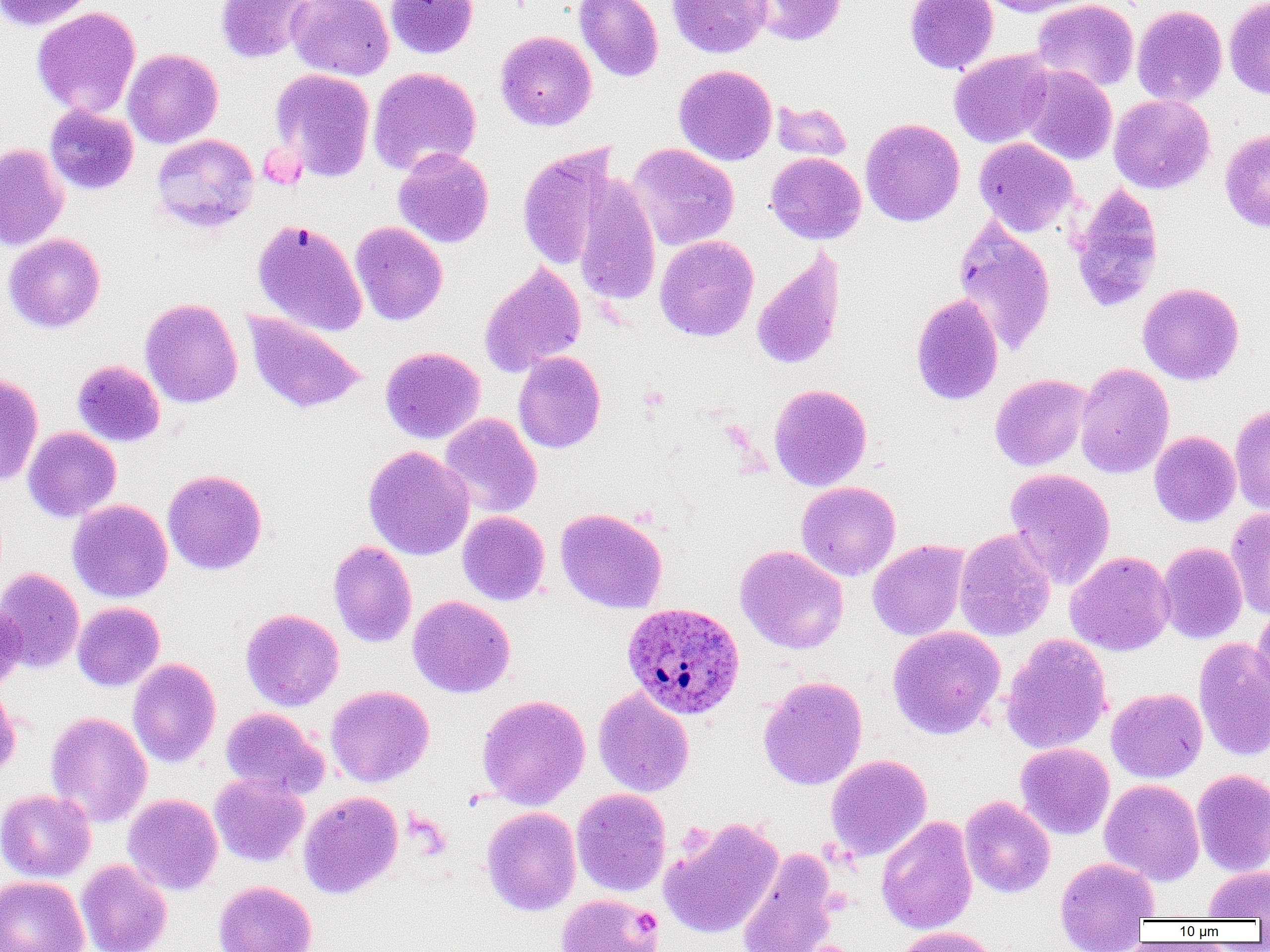

Approximate bounding boxes as [x1, y1, x2, y2] in pixels. Uninfected red blood cell locations: [0, 0, 97, 30], [215, 0, 314, 63], [286, 0, 394, 80], [385, 0, 478, 58], [574, 0, 664, 82], [667, 0, 770, 58], [746, 0, 846, 46], [904, 0, 997, 74], [975, 0, 1097, 17], [1032, 0, 1139, 92], [1224, 0, 1270, 98], [1132, 4, 1227, 106], [32, 7, 140, 118], [495, 30, 597, 131], [122, 48, 223, 148], [949, 49, 1055, 148], [674, 64, 777, 165], [1020, 65, 1117, 165], [368, 67, 481, 176], [270, 68, 375, 182], [1108, 94, 1215, 194], [771, 100, 852, 162], [44, 105, 138, 195], [860, 118, 965, 227], [1220, 129, 1270, 233], [151, 133, 259, 233], [974, 137, 1078, 236], [0, 143, 69, 251], [517, 143, 620, 271], [626, 143, 740, 251], [393, 147, 494, 248], [766, 152, 866, 244], [573, 174, 660, 306], [1070, 184, 1164, 313], [954, 217, 1056, 355], [253, 219, 368, 336], [350, 221, 448, 325], [3, 233, 105, 333], [655, 235, 759, 341], [752, 249, 845, 371], [479, 261, 586, 377], [1137, 282, 1245, 385], [911, 293, 1003, 406], [140, 297, 242, 408], [243, 310, 368, 414], [380, 346, 484, 444], [513, 351, 606, 453], [72, 360, 165, 447], [1074, 362, 1174, 479], [989, 373, 1093, 471], [0, 374, 43, 485], [769, 383, 872, 491], [1229, 404, 1270, 515], [439, 413, 542, 518], [23, 426, 121, 522], [1149, 431, 1240, 527], [363, 445, 474, 560], [1004, 467, 1116, 589], [162, 469, 267, 575], [796, 481, 901, 580], [68, 499, 173, 602], [555, 507, 668, 613], [1225, 507, 1270, 619], [457, 511, 550, 605], [954, 528, 1056, 642], [868, 539, 969, 641], [328, 541, 417, 647], [1157, 542, 1247, 644], [735, 545, 849, 655], [1065, 551, 1175, 656], [0, 567, 84, 673], [407, 595, 515, 697], [0, 601, 25, 691], [72, 601, 165, 691], [1252, 605, 1270, 711], [241, 608, 344, 711], [887, 625, 1005, 739], [1001, 633, 1113, 755], [1193, 637, 1270, 762], [128, 658, 221, 768], [757, 676, 868, 790], [0, 685, 21, 783], [326, 685, 434, 787], [593, 686, 695, 797], [1107, 688, 1207, 782], [477, 694, 591, 809], [220, 707, 329, 799], [45, 711, 152, 827], [1015, 742, 1115, 839], [826, 755, 932, 861], [1192, 769, 1270, 876], [209, 773, 309, 866], [1099, 779, 1204, 885], [571, 787, 671, 897], [0, 789, 96, 882], [299, 791, 403, 899], [123, 793, 223, 895], [960, 795, 1056, 897], [481, 806, 581, 916], [876, 815, 978, 935], [658, 816, 784, 939], [736, 848, 840, 952], [1054, 856, 1159, 949], [76, 859, 172, 952], [1203, 865, 1270, 920], [0, 875, 89, 952], [214, 881, 316, 952], [555, 893, 663, 952], [892, 926, 1003, 952]. Plasmodium ovale-infected red blood cell locations: [622, 601, 746, 720]. Slide-level diagnosis: Plasmodium ovale. Thin blood smear. Light microscopy. Captured at 1000x magnification. Single field of view. Image is 1270×952 pixels.